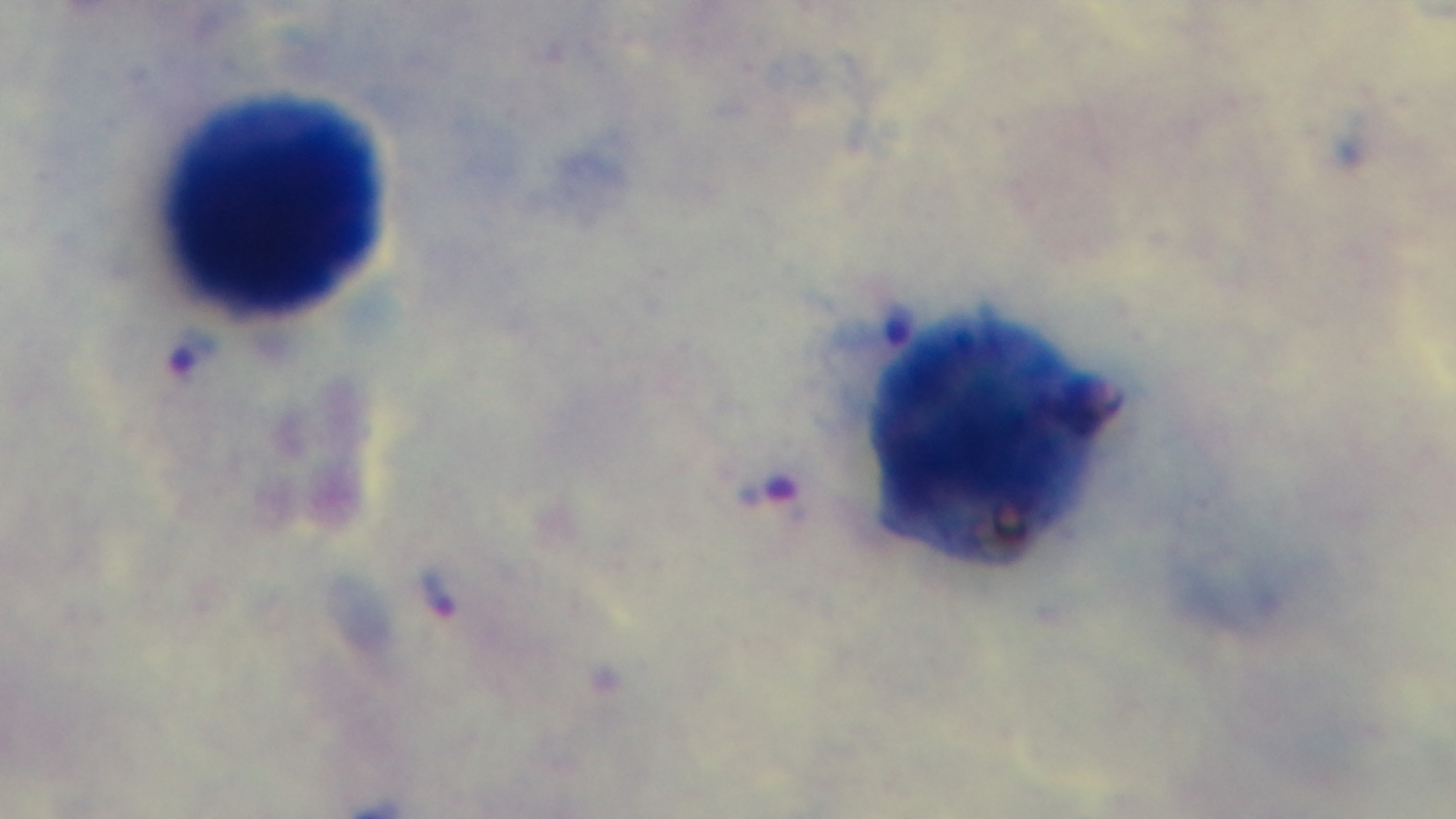 Preparation: thick blood film. Light microscopy. Oil-immersion objective, 100x. Giemsa stain. Malaria status: positive. Captured with a mounted 4K digital camera. Single field of view.